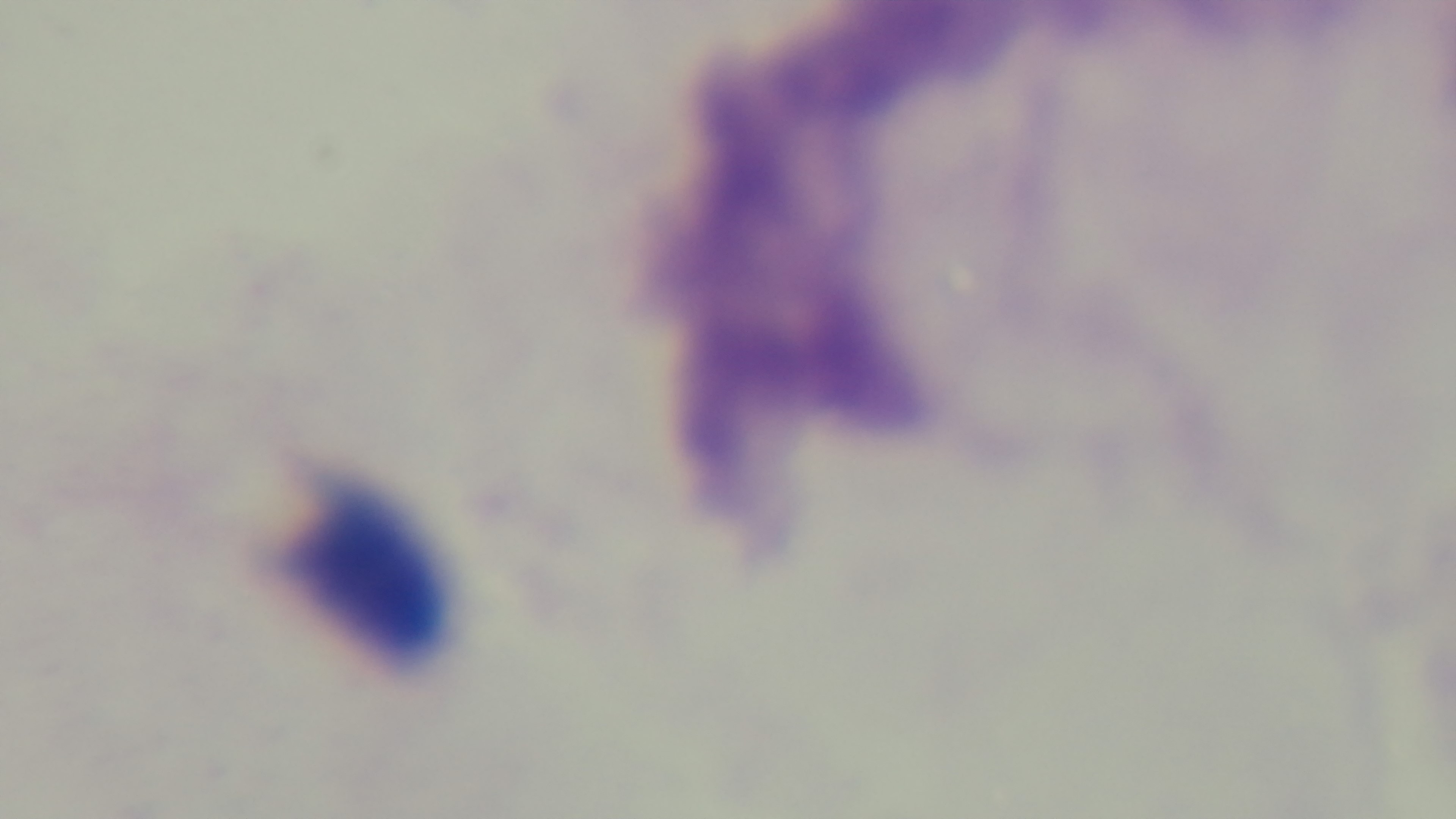
modality = light microscopy
malaria status = uninfected
preparation = thick
objective = 100x oil immersion
field of view = one from the slide
stain = Giemsa
capture = mounted 4K digital camera